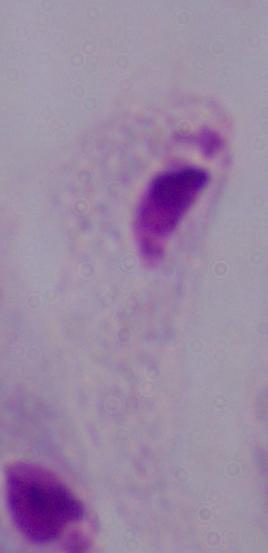
Summary:
  - Modality: micrograph
  - Magnification: 1000x
  - Identification: trichomonad